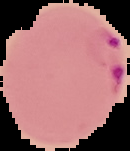

Summary:
  - Image type: segmented cell region with the area outside set to black
  - Preparation: thin blood film
  - Malaria status: parasitized
  - Image size: 130×151 pixels